Locate every leukocyte (white blood cell).
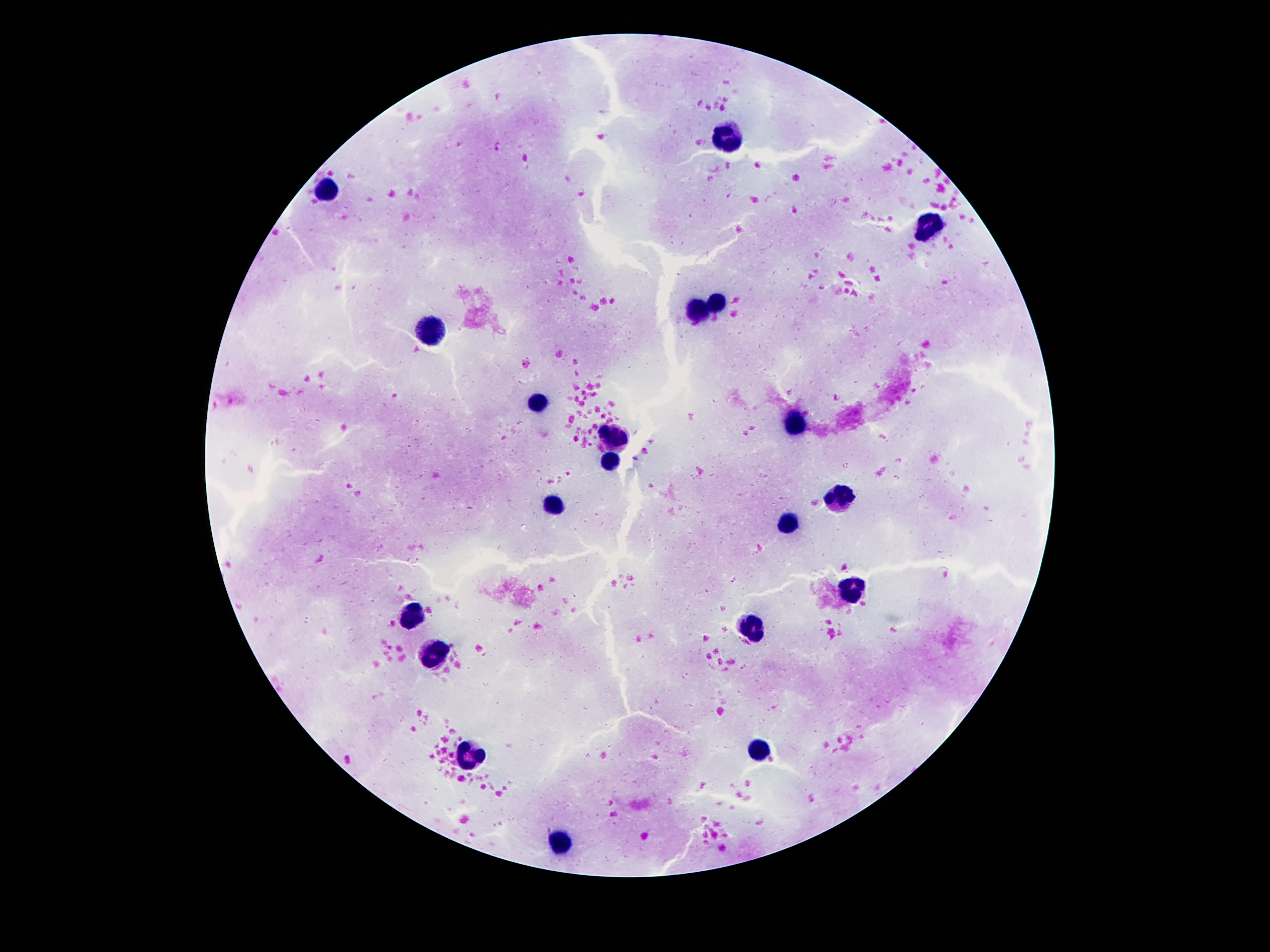

Approximate centers as (x, y) in pixels.
Leukocytes: (724, 137), (331, 192), (927, 228), (717, 301), (698, 308), (432, 330), (539, 402), (793, 423), (616, 437), (612, 461), (841, 496), (555, 505), (789, 526), (854, 590), (409, 615), (751, 627), (430, 655), (761, 747), (470, 757), (558, 842).

preparation = thick peripheral-blood smear
magnification = 100x
image size = 1270×952 pixels
capture = smartphone camera through the microscope eyepiece
field of view = one from this slide
stain = Giemsa
patient malaria status = uninfected